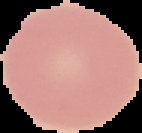

image_type: segmented cell region with the area outside set to black
result: negative for malaria parasites
image_size: 142×133 pixels
preparation: thin blood smear